Describe the morphology of the erythrocytes.
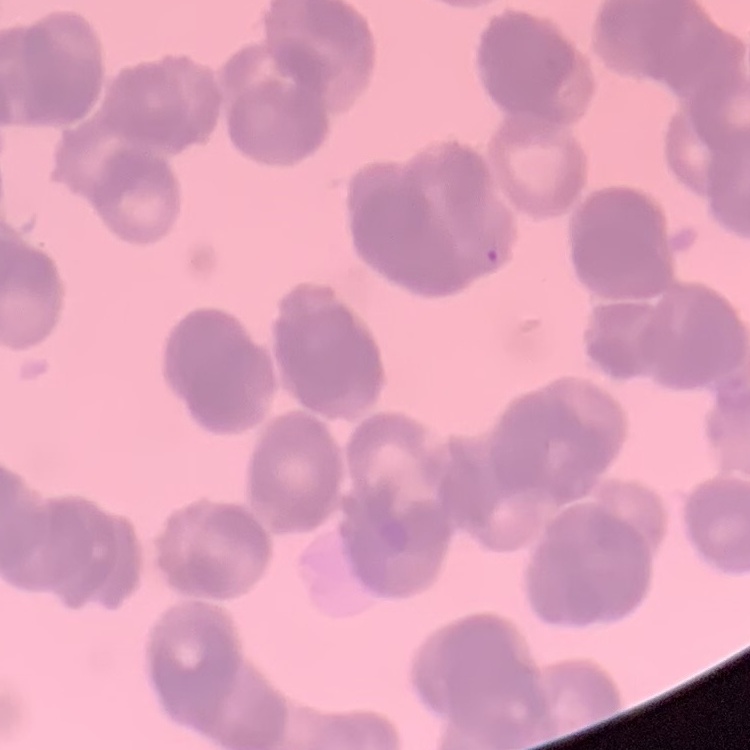

Rouleaux formation.

image type = square crop of a larger photomicrograph
stain = Field's or Giemsa
preparation = thin peripheral smear